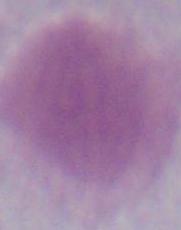

Summary:
  - Magnification: 1000x
  - Identification: red blood cell
  - Modality: micrograph